Describe the morphology of the red blood cells.
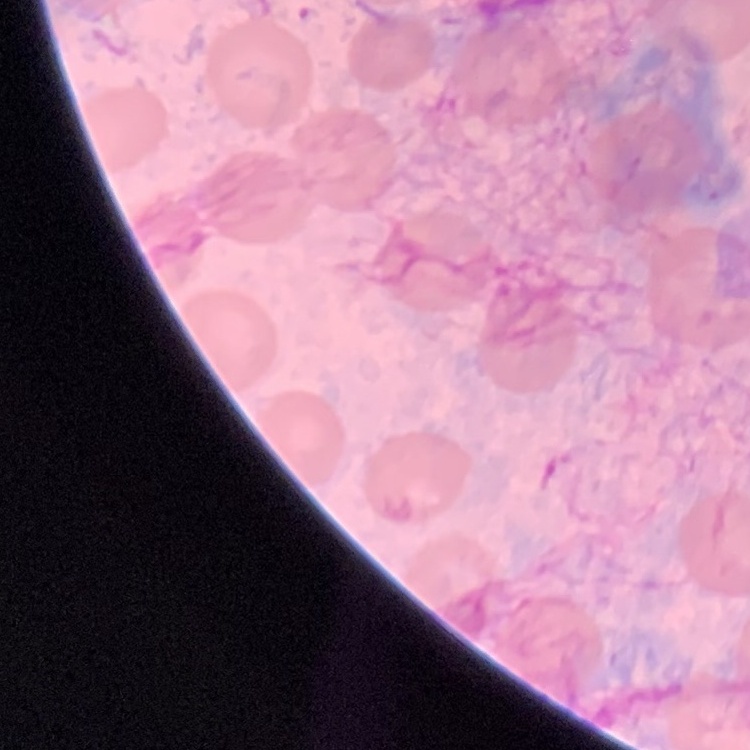

They show no rouleaux formation.

Summary:
  - Stain: Field's or Giemsa
  - Image type: square crop of a larger photomicrograph
  - Preparation: thin peripheral smear